Report the malaria status of this cell.
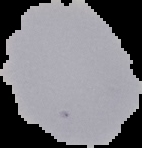

Uninfected.

Summary:
  - Image size: 142×148 pixels
  - Image type: cell region segmented out of the field of view; surrounding area masked to black
  - Preparation: thin blood smear